Assess this cell for malaria.
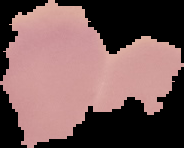

Uninfected.

{
  "image_type": "segmented cell region on a black background",
  "preparation": "thin blood smear",
  "image_size": "184×148 pixels"
}